Identify the parasite.
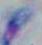

Toxoplasma gondii.

Captured at 1000x magnification. Micrograph.